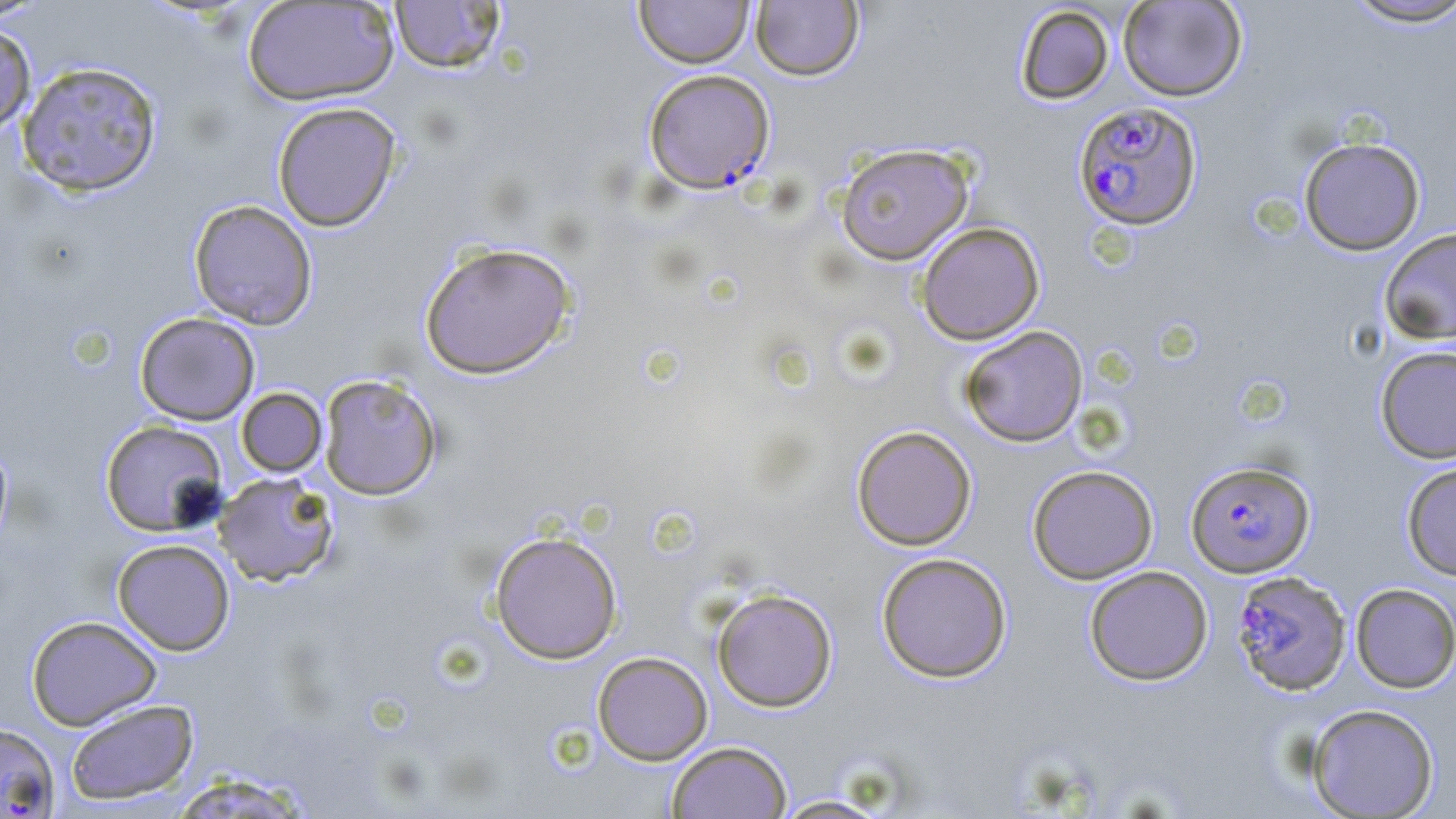

Summary:
  - Coordinate format: approximate bounding boxes as (x1, y1, x2, y2) in pixels
  - Plasmodium falciparum-infected red blood cell locations: (643, 68, 775, 194), (1073, 101, 1202, 231), (1185, 459, 1316, 578), (1231, 570, 1352, 696)
  - Uninfected red blood cell locations: (0, 0, 53, 24), (634, 0, 755, 68), (1117, 0, 1248, 101), (1342, 0, 1456, 29), (241, 1, 399, 106), (389, 1, 507, 74), (750, 1, 864, 81), (1015, 5, 1114, 104), (0, 24, 37, 137), (17, 60, 163, 197), (272, 101, 402, 232), (1298, 136, 1426, 255), (835, 143, 974, 265), (188, 199, 318, 330), (916, 221, 1045, 345), (1379, 226, 1456, 346), (418, 241, 576, 379), (134, 311, 260, 425), (959, 326, 1088, 447), (1375, 345, 1456, 464), (318, 373, 443, 501), (236, 387, 327, 477), (99, 420, 229, 537), (852, 425, 977, 550), (0, 437, 13, 555), (1401, 460, 1456, 581), (1027, 464, 1158, 584), (213, 472, 340, 587), (489, 530, 623, 664), (112, 538, 236, 655), (876, 552, 1012, 682), (1084, 565, 1213, 685), (1350, 583, 1456, 693), (711, 588, 838, 712), (25, 615, 162, 730), (592, 651, 713, 765), (65, 698, 199, 806), (1306, 703, 1440, 818), (0, 723, 61, 817), (667, 741, 793, 819), (164, 772, 317, 818), (767, 795, 895, 818)
  - Slide-level diagnosis: Plasmodium falciparum
  - Modality: optical microscopy
  - Image size: 1456×819 pixels
  - Preparation: thin blood smear
  - Stain: May-Grünwald-Giemsa
  - Magnification: 1000x
  - Field of view: single